State the preparation type.
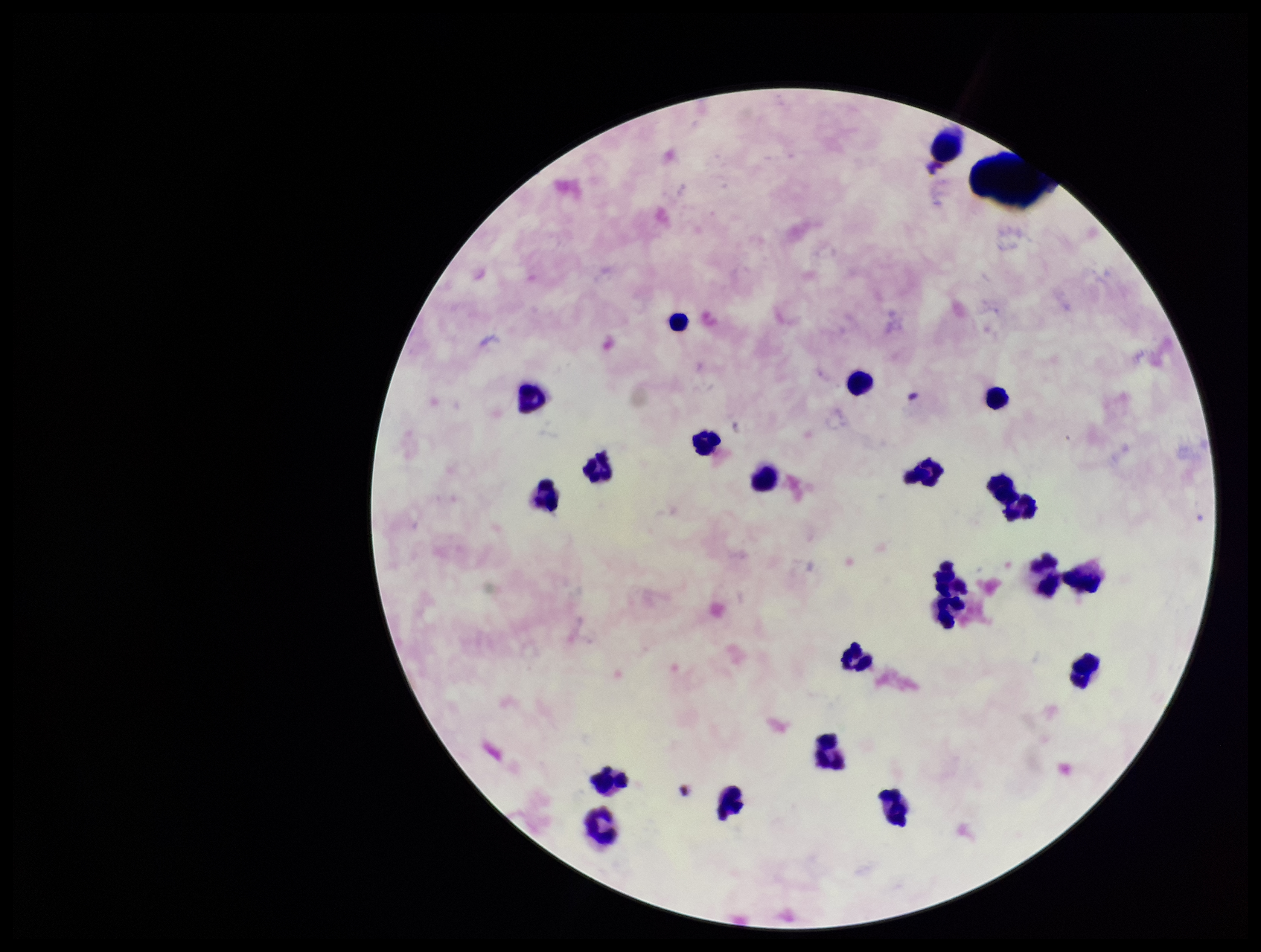
Thick.

Summary:
  - Capture: smartphone photograph through the microscope eyepiece
  - Stain: Giemsa
  - Image size: 1261×952 pixels
  - Patient malaria status: negative
  - Field of view: one from this slide
  - Parasite count: 0
  - Plasmodium parasites: none seen
  - Leukocyte count: 21